Classify this cell by malaria status.
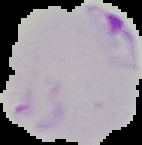
Parasitized.

Summary:
  - Image type: segmented cell region with the area outside set to black
  - Image size: 142×145 pixels
  - Preparation: thin blood smear